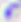
{
  "identification": "Toxoplasma gondii",
  "modality": "micrograph",
  "magnification": "400x"
}